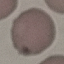

result = no malaria parasites seen
stain = Giemsa
preparation = thin blood smear
image type = cell patch, automatically extracted from a larger field of view and resized to 64 × 64 pixels
capture = smartphone camera at the microscope eyepiece